Outline each blood parasite and name the species.
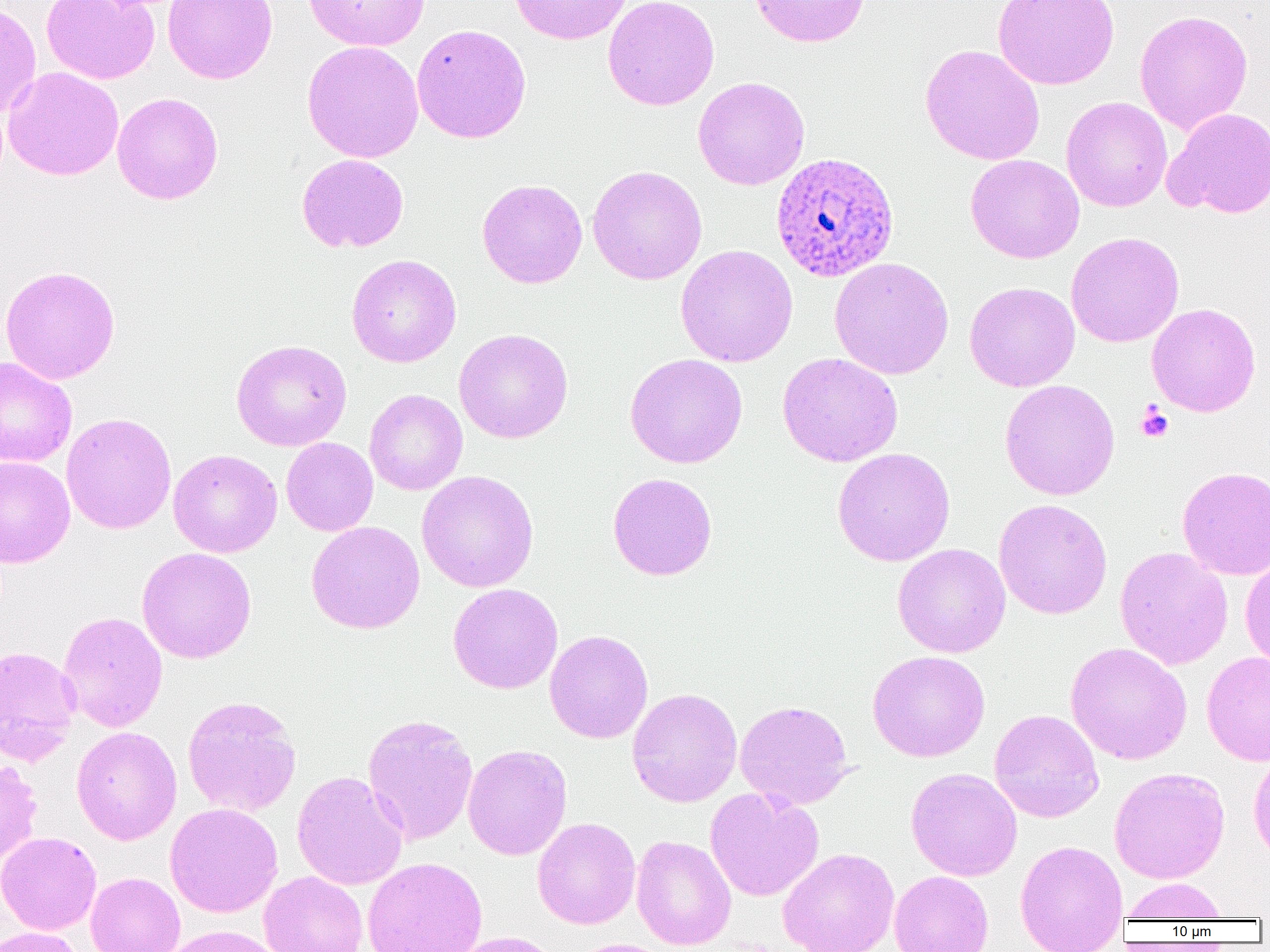
Approximate bounding boxes as (x1, y1, x2, y2) in pixels.
Plasmodium ovale-infected red blood cells: (770, 151, 899, 282).
No Plasmodium falciparum, Plasmodium malariae, Plasmodium vivax, Babesia divergens, or Trypanosoma brucei observed.

Platelet locations: (1136, 403, 1174, 442). Uninfected red blood cell locations: (40, 0, 160, 84), (163, 0, 278, 84), (302, 0, 429, 51), (508, 0, 632, 45), (602, 0, 720, 110), (749, 0, 870, 47), (993, 0, 1119, 90), (0, 2, 42, 120), (1134, 10, 1253, 134), (411, 24, 532, 144), (302, 40, 424, 163), (920, 44, 1045, 166), (2, 67, 124, 180), (692, 76, 810, 190), (112, 92, 224, 204), (1061, 96, 1172, 212), (1163, 107, 1270, 219), (296, 154, 409, 253), (965, 154, 1084, 263), (587, 165, 707, 285), (477, 179, 587, 288), (1066, 232, 1184, 347), (675, 244, 798, 367), (346, 254, 461, 367), (829, 257, 954, 380), (0, 265, 120, 385), (964, 281, 1080, 391), (1146, 303, 1261, 417), (453, 328, 573, 444), (231, 339, 352, 451), (624, 353, 748, 468), (777, 353, 903, 467), (0, 357, 77, 467), (999, 378, 1120, 501), (364, 389, 467, 495), (61, 412, 176, 534), (281, 437, 378, 536), (832, 447, 955, 566), (168, 449, 282, 558), (0, 456, 75, 568), (1177, 465, 1270, 579), (416, 470, 539, 593), (607, 472, 718, 580), (993, 498, 1113, 619), (305, 521, 425, 634), (892, 543, 1011, 657), (1114, 546, 1233, 670), (136, 547, 257, 664), (1240, 556, 1270, 671), (448, 583, 563, 694), (57, 611, 168, 732), (544, 630, 653, 743), (1066, 642, 1192, 765), (0, 646, 81, 764), (867, 650, 990, 762), (1202, 651, 1270, 766), (627, 687, 742, 807), (181, 695, 302, 817), (734, 699, 854, 810), (989, 709, 1104, 823), (362, 713, 478, 845), (71, 726, 182, 845), (463, 744, 572, 860), (1248, 748, 1270, 866), (0, 758, 43, 865), (906, 767, 1022, 881), (1109, 767, 1230, 884), (291, 770, 408, 890), (705, 787, 824, 902), (165, 802, 283, 918), (532, 817, 641, 929), (0, 831, 101, 934), (631, 835, 737, 950), (1015, 839, 1128, 952), (778, 847, 899, 952), (362, 857, 488, 952), (259, 871, 368, 952), (889, 871, 994, 952), (85, 872, 185, 952), (1122, 877, 1230, 921), (162, 925, 284, 952), (0, 926, 85, 952), (449, 931, 563, 952), (566, 938, 679, 952). Slide-level diagnosis: Plasmodium ovale. Optical microscopy. Thin blood smear. 1000x magnification. Image is 1270×952 pixels. One field of a larger specimen.